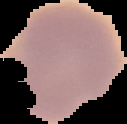
Summary:
  - Image size: 127×124 pixels
  - Preparation: thin blood film
  - Malaria status: uninfected
  - Image type: cell region segmented out of the field of view; surrounding area masked to black